Outline each Plasmodium ovale-infected red blood cell.
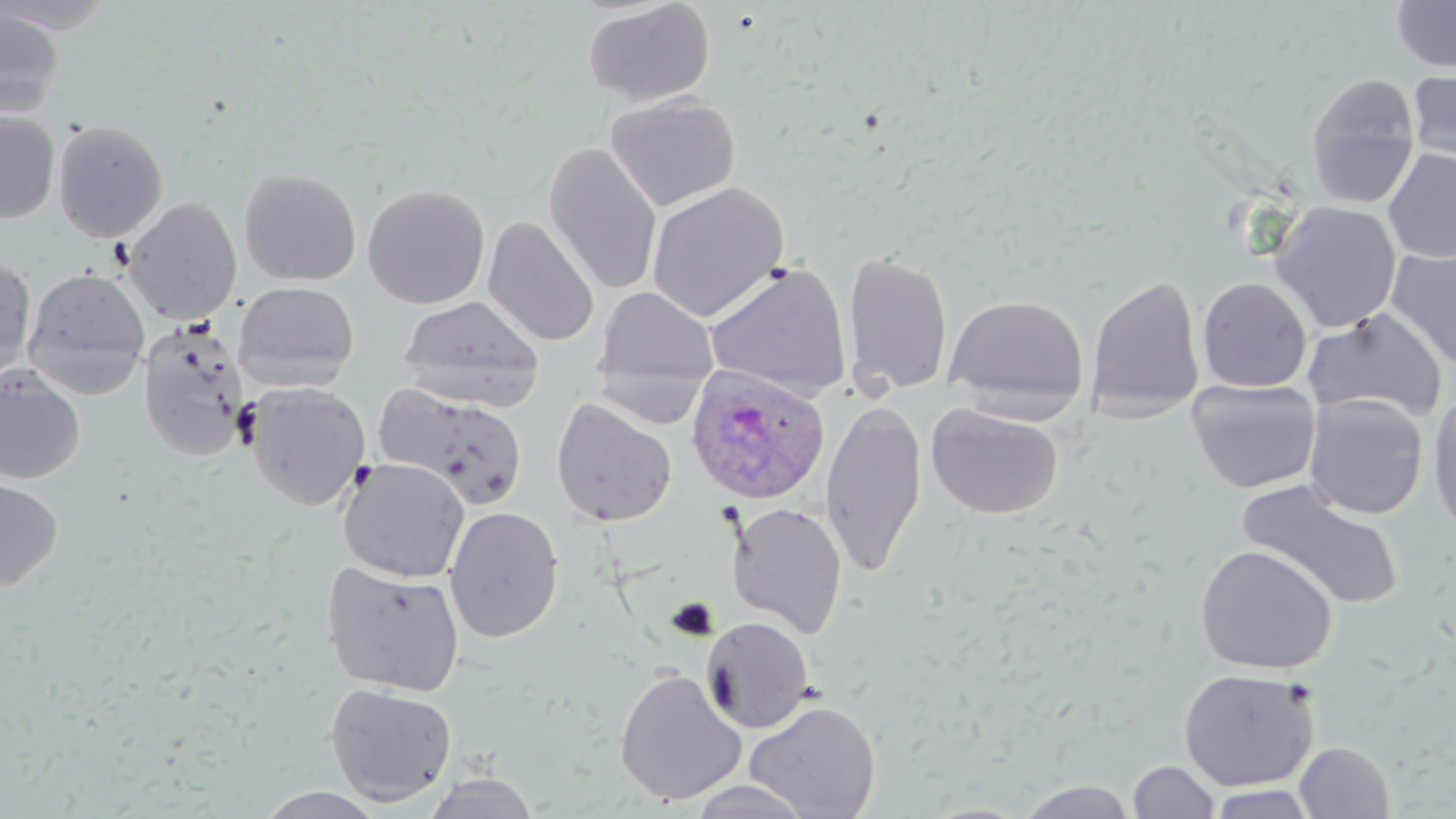
Approximate bounding boxes as (x1,y1)-(x2,y2) corner pairs in pixels.
Plasmodium ovale-infected red blood cells: (685,365)-(831,505).

Summary:
  - Uninfected red blood cell locations: (582,0)-(716,107), (1391,0)-(1456,72), (0,4)-(64,118), (1406,69)-(1456,165), (1305,73)-(1421,208), (605,93)-(740,212), (0,111)-(60,223), (52,119)-(169,242), (542,142)-(664,296), (1383,148)-(1456,263), (239,168)-(362,286), (646,182)-(790,322), (362,184)-(490,309), (123,197)-(242,325), (1270,201)-(1402,333), (482,216)-(600,347), (842,249)-(953,397), (1386,249)-(1456,370), (0,256)-(37,380), (703,261)-(852,400), (22,268)-(150,398), (1085,274)-(1205,420), (1197,277)-(1312,393), (233,280)-(360,392), (593,286)-(720,396), (944,294)-(1088,416), (398,295)-(544,409), (1303,308)-(1448,424), (137,320)-(250,462), (0,368)-(85,485), (1186,378)-(1321,493), (245,382)-(371,511), (374,383)-(531,511), (1427,393)-(1456,536), (1303,394)-(1428,519), (551,397)-(676,527), (820,400)-(928,578), (926,402)-(1064,520), (337,458)-(470,583), (0,477)-(63,591), (1238,480)-(1405,610), (726,502)-(848,638), (444,506)-(564,643), (1195,544)-(1338,675), (321,561)-(466,696), (700,616)-(814,734), (613,667)-(746,806), (1178,668)-(1319,792), (324,681)-(458,807), (744,700)-(881,818), (1294,741)-(1395,818), (1128,760)-(1220,818), (421,772)-(541,818), (683,779)-(818,818), (1017,780)-(1137,819), (1205,784)-(1319,818), (255,787)-(387,818)
  - Slide-level diagnosis: Plasmodium ovale
  - Stain: May-Grünwald-Giemsa
  - Modality: optical microscopy
  - Image size: 1456×819 pixels
  - Magnification: 1000x
  - Preparation: thin blood smear
  - Field of view: one of a larger specimen